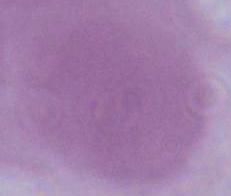

modality: micrograph
identification: erythrocyte
magnification: 1000x